Name the parasite shown.
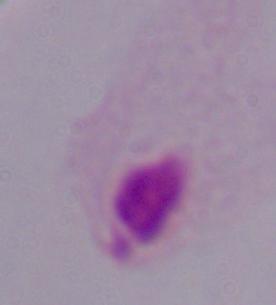
A trichomonad.

Summary:
  - Modality: micrograph
  - Magnification: 1000x